Classify this cell by malaria status.
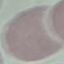

Uninfected.

Summary:
  - Image type: automatically extracted cell patch, resized to 64 × 64 pixels
  - Stain: Giemsa
  - Preparation: thin blood film
  - Capture: smartphone through the microscope eyepiece